Identify the cell.
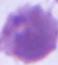
This is an erythrocyte.

modality: photomicrograph
magnification: 1000x